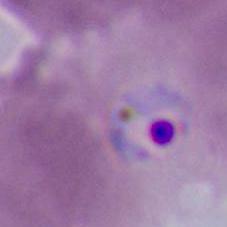
Captured at either 400x or 1000x magnification. A Plasmodium parasite is shown. Photomicrograph.